State the preparation type.
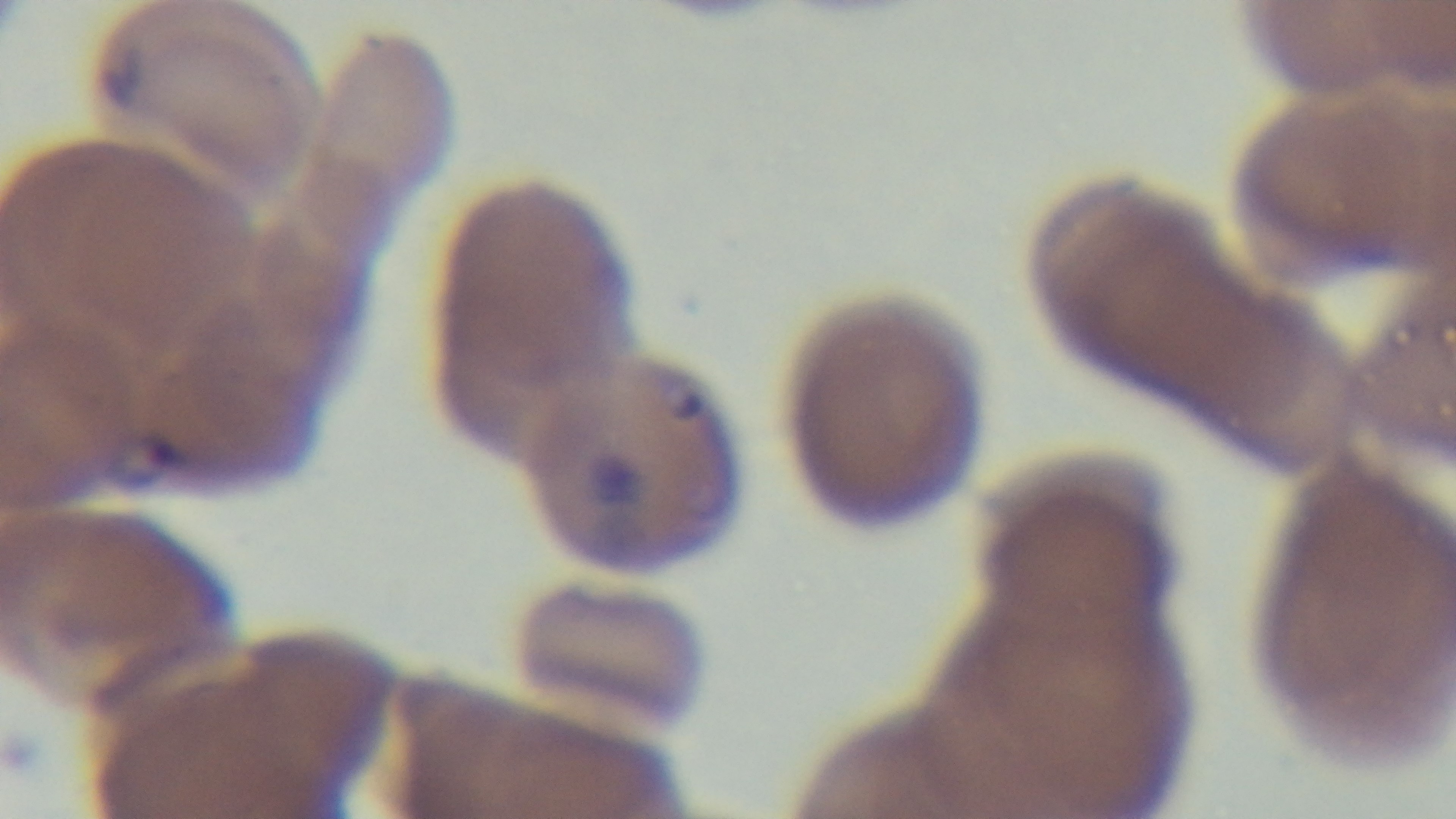
A thin smear.

malaria status = positive
stain = Giemsa
modality = light microscopy
objective = 100x oil immersion
capture = mounted 4K digital camera
field of view = one from the slide